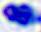

modality = micrograph
identification = leukocyte
magnification = 400x